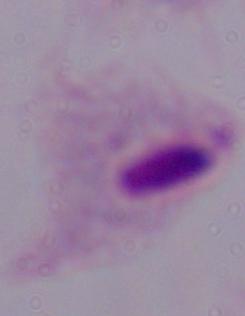
magnification = 1000x
identification = trichomonad
modality = photomicrograph